Mark where platelets are.
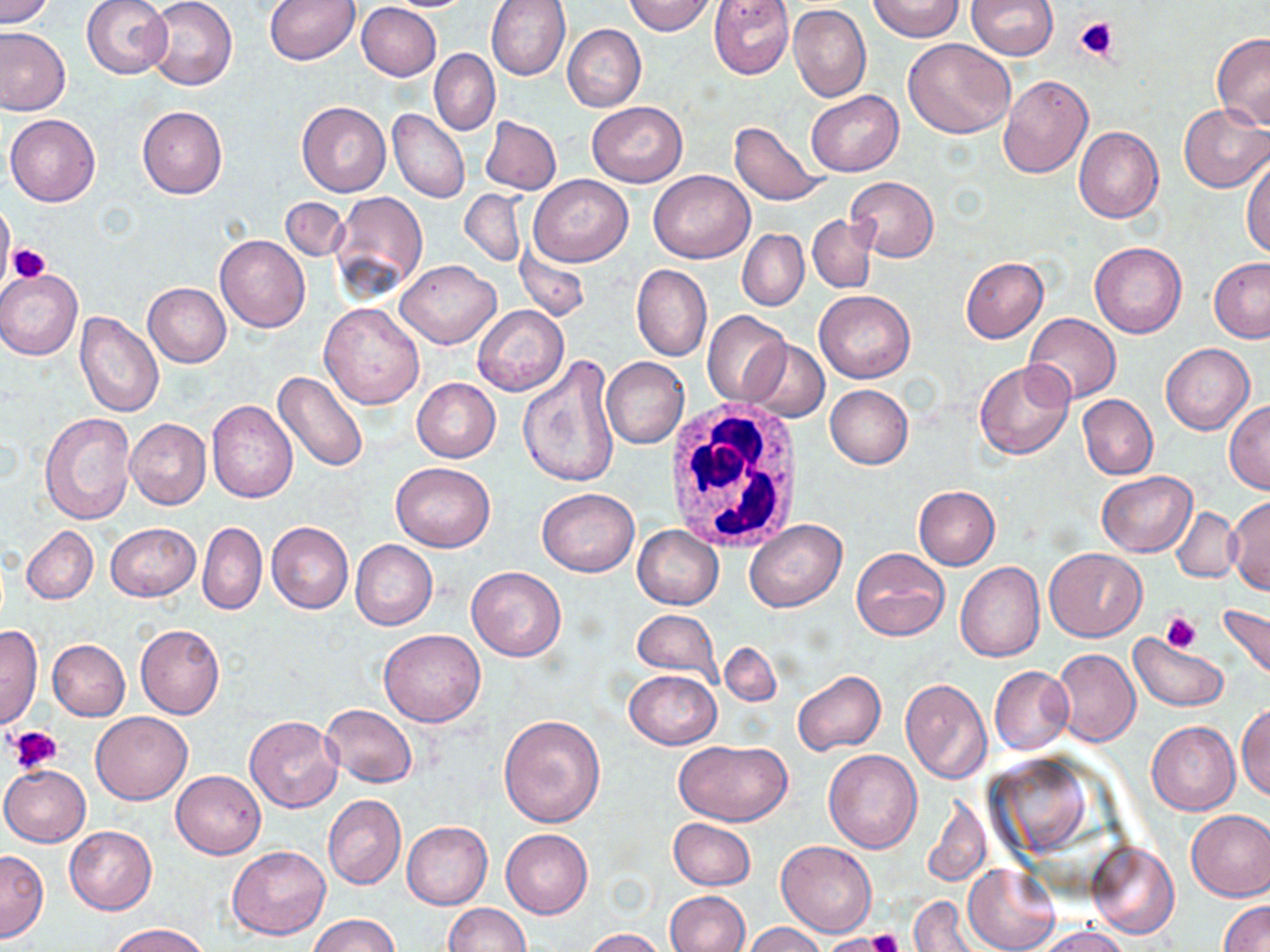
Approximate bounding boxes as named x1/y1/x2/y2 corners in pixels.
Platelets: (x1=1076, y1=17, x2=1119, y2=63), (x1=8, y1=244, x2=50, y2=283), (x1=1161, y1=611, x2=1200, y2=653), (x1=7, y1=725, x2=62, y2=775), (x1=866, y1=928, x2=907, y2=952), (x1=826, y1=933, x2=894, y2=952).

White blood cell locations: (x1=659, y1=401, x2=809, y2=549). Uninfected red blood cell locations: (x1=0, y1=0, x2=56, y2=27), (x1=81, y1=0, x2=172, y2=78), (x1=147, y1=0, x2=238, y2=89), (x1=264, y1=0, x2=360, y2=65), (x1=380, y1=0, x2=476, y2=11), (x1=486, y1=0, x2=571, y2=80), (x1=623, y1=0, x2=718, y2=35), (x1=709, y1=0, x2=794, y2=79), (x1=871, y1=0, x2=963, y2=41), (x1=967, y1=1, x2=1058, y2=60), (x1=357, y1=3, x2=442, y2=81), (x1=788, y1=3, x2=871, y2=101), (x1=563, y1=24, x2=647, y2=112), (x1=0, y1=27, x2=72, y2=116), (x1=1212, y1=34, x2=1270, y2=130), (x1=903, y1=38, x2=1015, y2=139), (x1=430, y1=50, x2=501, y2=135), (x1=998, y1=75, x2=1093, y2=179), (x1=806, y1=89, x2=903, y2=175), (x1=297, y1=101, x2=391, y2=197), (x1=587, y1=101, x2=687, y2=187), (x1=1179, y1=104, x2=1270, y2=193), (x1=137, y1=105, x2=228, y2=199), (x1=388, y1=109, x2=469, y2=203), (x1=6, y1=113, x2=100, y2=207), (x1=480, y1=115, x2=561, y2=195), (x1=728, y1=120, x2=829, y2=206), (x1=1074, y1=126, x2=1163, y2=223), (x1=1242, y1=152, x2=1270, y2=257), (x1=649, y1=170, x2=754, y2=263), (x1=527, y1=174, x2=634, y2=266), (x1=846, y1=176, x2=938, y2=262), (x1=460, y1=189, x2=526, y2=265), (x1=330, y1=190, x2=427, y2=301), (x1=281, y1=196, x2=349, y2=261), (x1=0, y1=201, x2=15, y2=286), (x1=807, y1=215, x2=876, y2=292), (x1=737, y1=229, x2=809, y2=311), (x1=214, y1=234, x2=310, y2=332), (x1=5, y1=237, x2=47, y2=290), (x1=1090, y1=242, x2=1186, y2=338), (x1=515, y1=244, x2=590, y2=322), (x1=961, y1=257, x2=1048, y2=343), (x1=1209, y1=257, x2=1270, y2=342), (x1=396, y1=260, x2=500, y2=349), (x1=632, y1=265, x2=712, y2=362), (x1=1, y1=269, x2=82, y2=360), (x1=142, y1=282, x2=231, y2=367), (x1=815, y1=291, x2=914, y2=383), (x1=319, y1=303, x2=425, y2=409), (x1=472, y1=306, x2=567, y2=396), (x1=75, y1=310, x2=164, y2=416), (x1=702, y1=311, x2=792, y2=407), (x1=1025, y1=312, x2=1120, y2=403), (x1=743, y1=340, x2=830, y2=421), (x1=1162, y1=343, x2=1254, y2=435), (x1=515, y1=354, x2=622, y2=488), (x1=602, y1=357, x2=690, y2=448), (x1=974, y1=360, x2=1074, y2=459), (x1=273, y1=370, x2=370, y2=473), (x1=411, y1=377, x2=501, y2=462), (x1=824, y1=384, x2=913, y2=469), (x1=1077, y1=394, x2=1158, y2=479), (x1=207, y1=399, x2=297, y2=503), (x1=1225, y1=400, x2=1270, y2=495), (x1=40, y1=412, x2=135, y2=523), (x1=125, y1=419, x2=212, y2=509), (x1=390, y1=461, x2=495, y2=551), (x1=1097, y1=470, x2=1197, y2=557), (x1=913, y1=485, x2=1000, y2=570), (x1=537, y1=488, x2=640, y2=577), (x1=1226, y1=496, x2=1270, y2=595), (x1=1173, y1=507, x2=1240, y2=582), (x1=744, y1=519, x2=847, y2=613), (x1=197, y1=521, x2=266, y2=615), (x1=266, y1=522, x2=354, y2=613), (x1=105, y1=523, x2=201, y2=601), (x1=22, y1=526, x2=98, y2=605), (x1=633, y1=526, x2=722, y2=609), (x1=350, y1=539, x2=438, y2=630), (x1=851, y1=547, x2=949, y2=642), (x1=1044, y1=548, x2=1146, y2=641), (x1=955, y1=562, x2=1046, y2=662), (x1=465, y1=566, x2=566, y2=661), (x1=1220, y1=603, x2=1270, y2=680), (x1=632, y1=610, x2=720, y2=679), (x1=134, y1=622, x2=225, y2=720), (x1=0, y1=624, x2=43, y2=731), (x1=378, y1=629, x2=486, y2=727), (x1=1129, y1=633, x2=1229, y2=712), (x1=48, y1=639, x2=130, y2=720), (x1=720, y1=642, x2=780, y2=706), (x1=1051, y1=648, x2=1141, y2=747), (x1=989, y1=666, x2=1075, y2=755), (x1=624, y1=669, x2=720, y2=749), (x1=792, y1=670, x2=887, y2=756), (x1=899, y1=678, x2=993, y2=785), (x1=321, y1=703, x2=418, y2=788), (x1=1237, y1=703, x2=1270, y2=801), (x1=90, y1=711, x2=192, y2=804), (x1=498, y1=713, x2=605, y2=828), (x1=245, y1=716, x2=343, y2=814), (x1=1146, y1=721, x2=1240, y2=815), (x1=674, y1=739, x2=794, y2=827), (x1=822, y1=749, x2=923, y2=853), (x1=0, y1=765, x2=90, y2=847), (x1=171, y1=771, x2=265, y2=858), (x1=922, y1=792, x2=991, y2=887), (x1=323, y1=795, x2=406, y2=889), (x1=1186, y1=810, x2=1270, y2=901), (x1=668, y1=817, x2=755, y2=890), (x1=402, y1=821, x2=493, y2=909), (x1=65, y1=825, x2=157, y2=914), (x1=501, y1=828, x2=592, y2=918), (x1=777, y1=840, x2=876, y2=937), (x1=1086, y1=841, x2=1179, y2=940), (x1=228, y1=846, x2=330, y2=940), (x1=0, y1=850, x2=48, y2=941), (x1=963, y1=864, x2=1058, y2=952), (x1=665, y1=891, x2=750, y2=952), (x1=908, y1=895, x2=977, y2=951), (x1=1219, y1=900, x2=1270, y2=952), (x1=442, y1=903, x2=530, y2=952), (x1=309, y1=913, x2=400, y2=952), (x1=109, y1=922, x2=210, y2=952), (x1=743, y1=922, x2=828, y2=952), (x1=1036, y1=925, x2=1131, y2=952), (x1=583, y1=928, x2=665, y2=952), (x1=820, y1=933, x2=894, y2=952). Slide-level diagnosis: no evidence of blood parasites. 1000x magnification. Image is 1270×952 pixels. May-Grünwald-Giemsa-stained preparation. Thin blood film. Light microscopy. One field of a larger specimen.